Describe the morphology of the red blood cells.
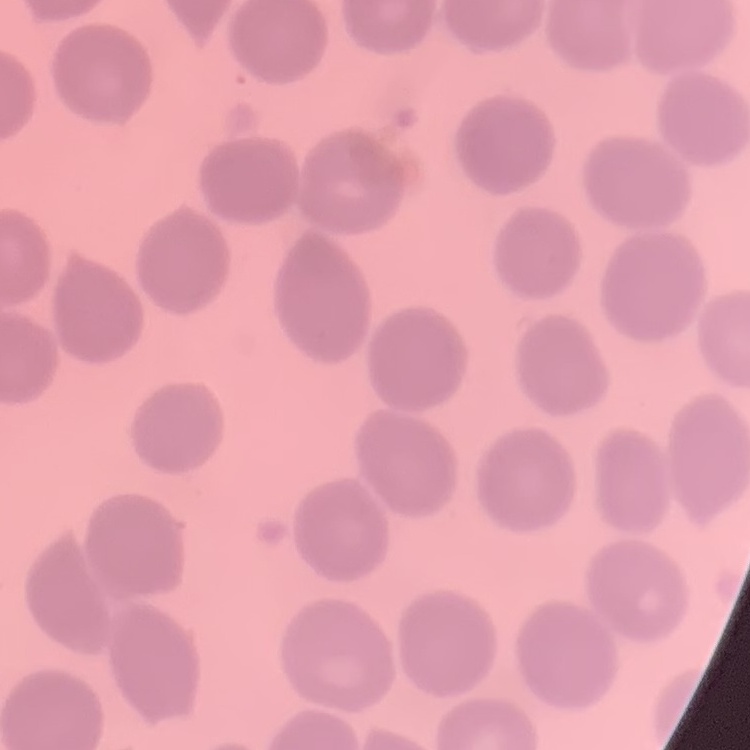
They show no rouleaux formation.

Square crop of a larger photomicrograph. Thin peripheral smear. Field's or Giemsa stain.